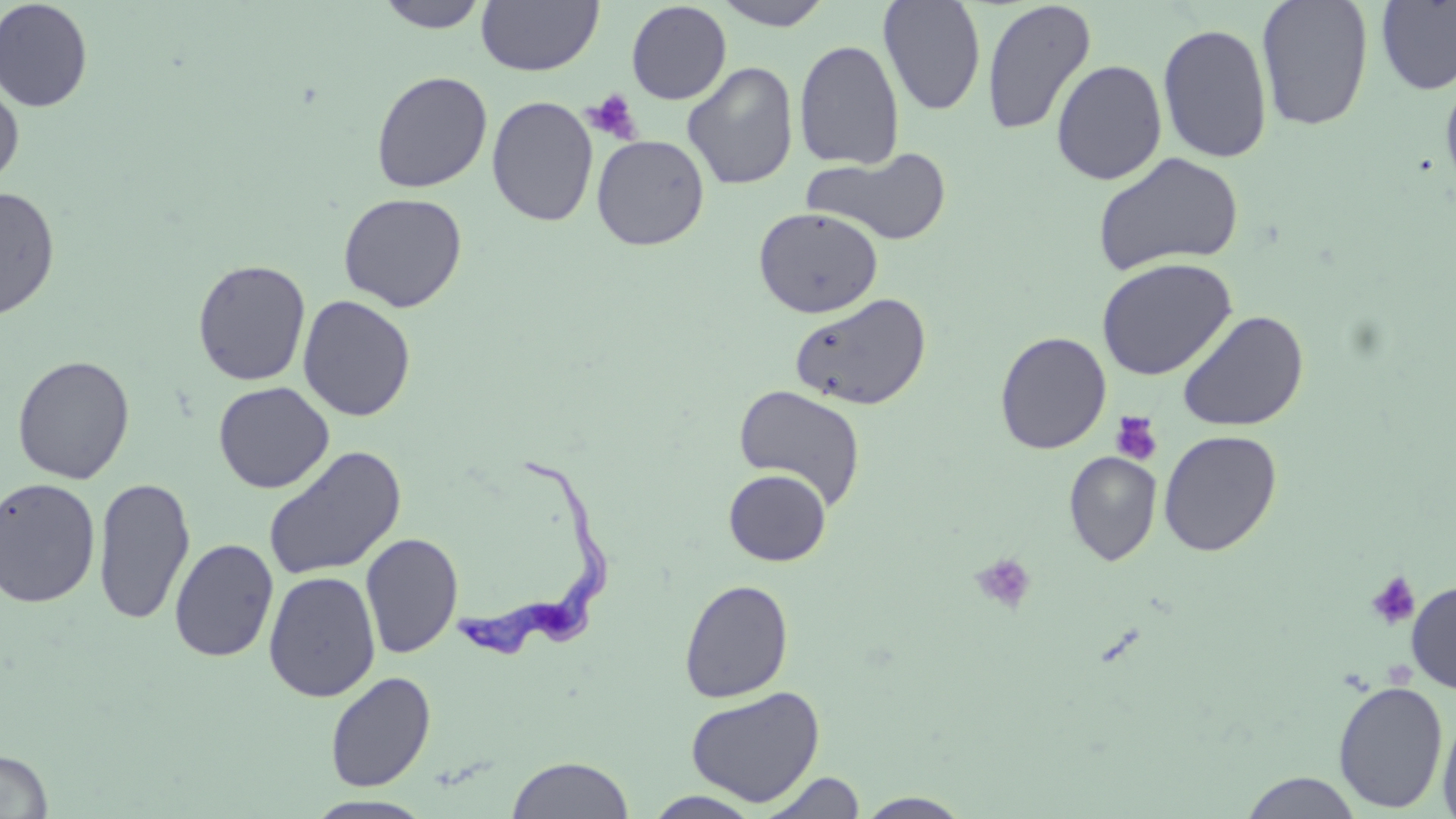
slide-level diagnosis = Trypanosoma brucei
stain = May-Grünwald-Giemsa
uninfected red blood cell locations = approximate bounding boxes as [x1, y1, x2, y2] in pixels: [0, 0, 94, 112], [376, 0, 490, 32], [717, 0, 832, 30], [879, 0, 987, 116], [1256, 0, 1374, 132], [1375, 0, 1456, 96], [475, 1, 604, 76], [626, 1, 731, 104], [980, 1, 1097, 136], [1157, 22, 1272, 164], [794, 39, 905, 170], [1051, 59, 1167, 185], [682, 61, 799, 190], [1439, 69, 1456, 202], [370, 70, 493, 193], [0, 79, 24, 190], [487, 95, 599, 227], [591, 134, 709, 250], [803, 147, 952, 247], [1092, 151, 1244, 277], [0, 187, 60, 320], [338, 192, 468, 312], [753, 207, 884, 318], [1096, 257, 1238, 380], [192, 259, 311, 386], [790, 292, 932, 410], [298, 295, 416, 421], [1177, 310, 1309, 432], [994, 331, 1112, 454], [12, 355, 135, 485], [213, 382, 334, 493], [733, 384, 865, 509], [1158, 429, 1282, 557], [263, 446, 407, 581], [1064, 451, 1162, 566], [723, 468, 832, 566], [0, 477, 101, 609], [92, 477, 195, 625], [360, 532, 463, 659], [169, 538, 279, 662], [263, 570, 381, 703], [679, 579, 794, 703], [1406, 579, 1456, 694], [324, 671, 436, 792], [1332, 679, 1449, 813], [685, 685, 825, 806], [1437, 709, 1456, 819], [0, 749, 53, 818], [507, 756, 634, 818], [760, 771, 867, 818], [1239, 772, 1365, 818], [644, 790, 764, 818], [855, 792, 973, 818], [303, 795, 437, 818]
platelet locations = approximate bounding boxes as [x1, y1, x2, y2] in pixels: [583, 90, 642, 144], [1111, 411, 1163, 466], [971, 552, 1038, 615], [1365, 571, 1421, 630]
modality = optical microscopy
image size = 1456×819 pixels
preparation = thin blood smear
field of view = one of a larger specimen
Trypanosoma brucei locations = approximate bounding boxes as [x1, y1, x2, y2] in pixels: [455, 455, 610, 660]
magnification = 1000x